Point out each Plasmodium parasite and each leukocyte.
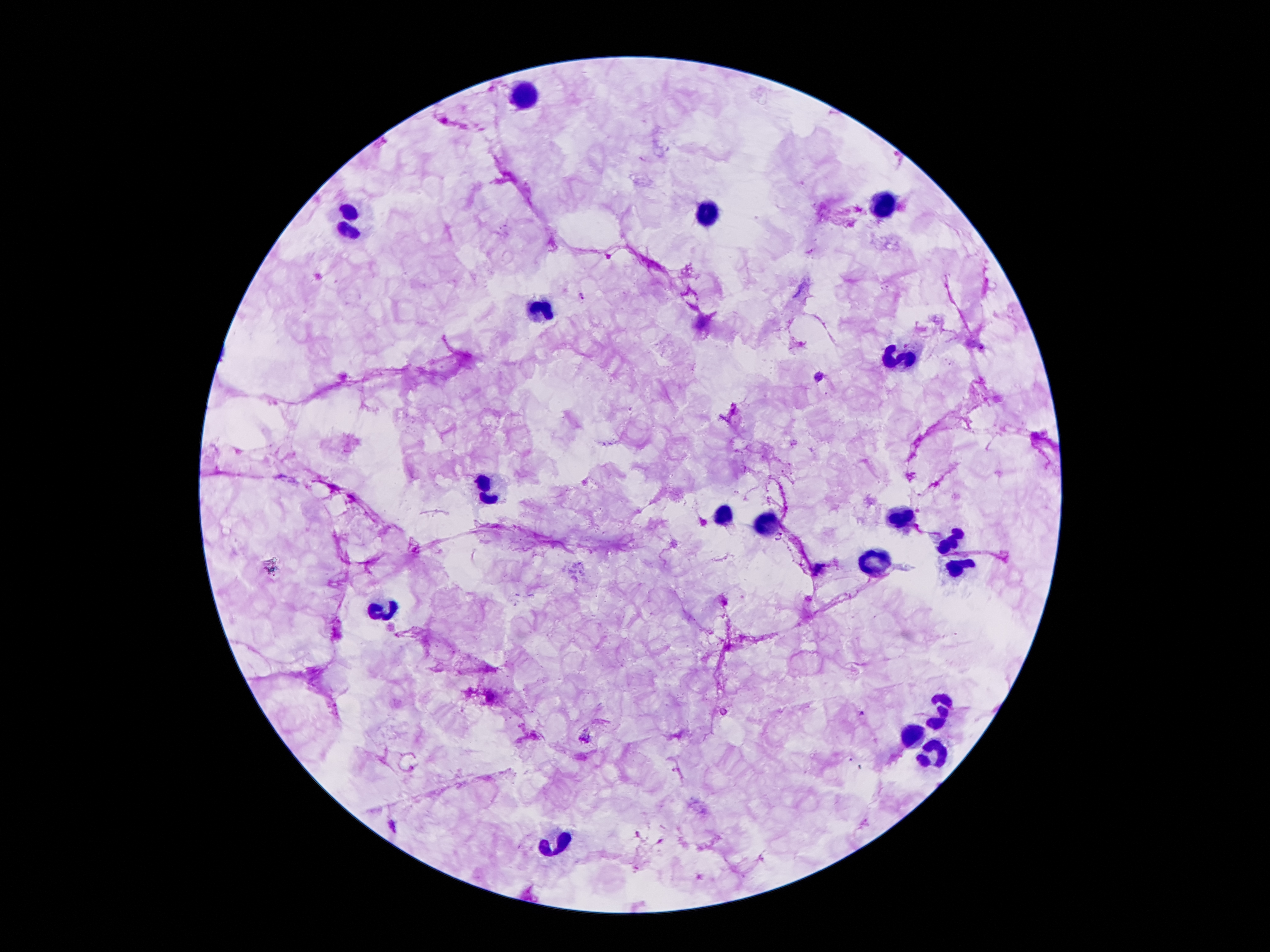

Approximate object centers, in pixels from the top-left corner.
Plasmodium parasites: (x=582, y=296), (x=818, y=377), (x=862, y=713), (x=585, y=736).
Leukocytes: (x=523, y=93), (x=886, y=203), (x=707, y=214), (x=348, y=222), (x=539, y=309), (x=899, y=362), (x=479, y=490), (x=722, y=516), (x=906, y=518), (x=766, y=524), (x=945, y=541), (x=875, y=565), (x=961, y=570), (x=388, y=610).

Summary:
  - Preparation: thick peripheral-blood smear
  - Field of view: single
  - Stain: Giemsa
  - Image size: 1270×952 pixels
  - Magnification: 100x
  - Capture: smartphone camera through the microscope eyepiece
  - Patient malaria status: infected with Plasmodium falciparum